Locate every blood parasite and identify its species.
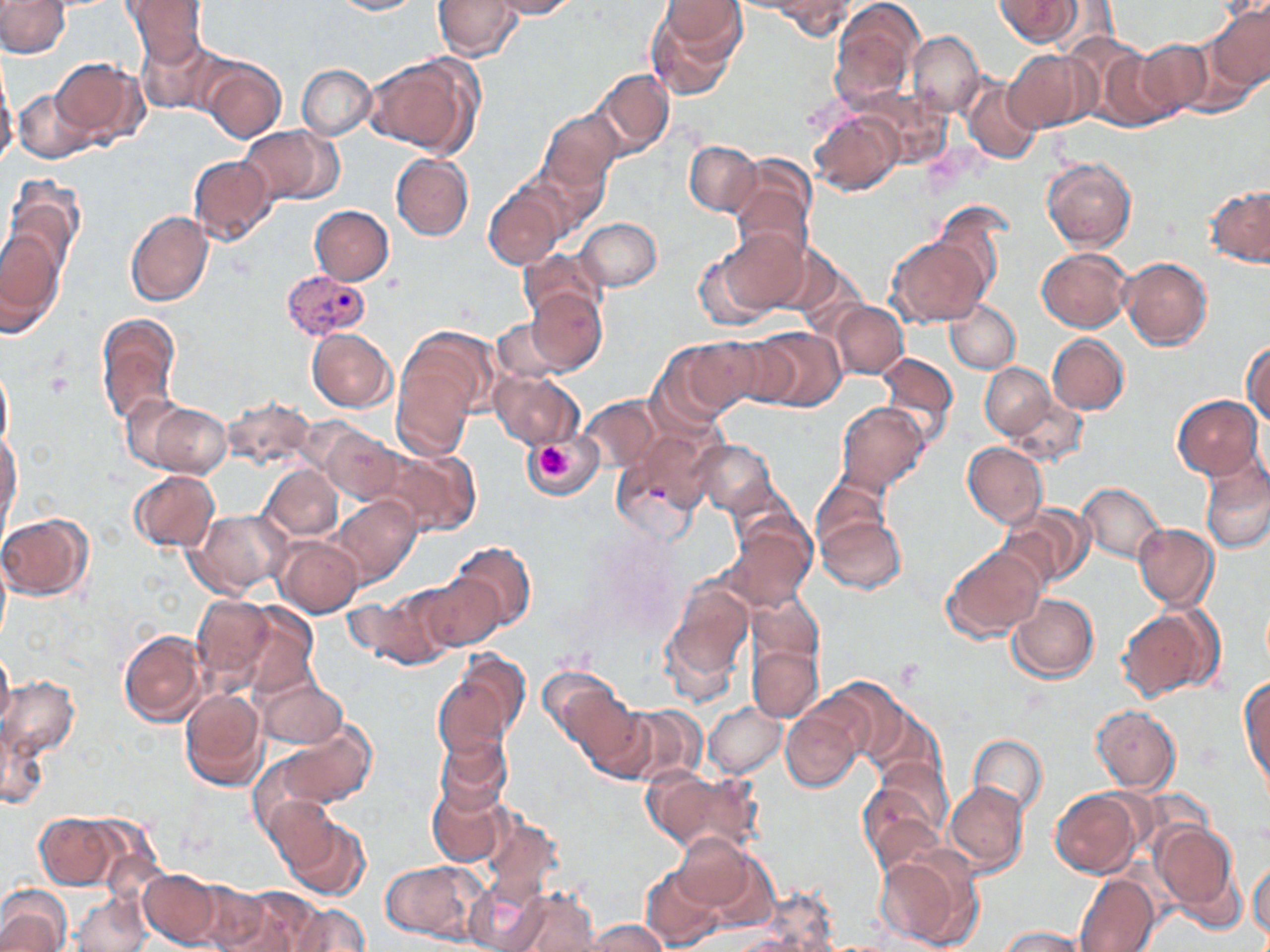
Approximate bounding boxes as named x1/y1/x2/y2 corners in pixels.
Plasmodium vivax-infected red blood cells: (x1=282, y1=269, x2=372, y2=343).
No Plasmodium falciparum, Plasmodium ovale, Plasmodium malariae, Babesia divergens, or Trypanosoma brucei observed.

Summary:
  - Uninfected red blood cell locations: (x1=0, y1=0, x2=70, y2=57), (x1=121, y1=0, x2=211, y2=64), (x1=434, y1=0, x2=523, y2=61), (x1=486, y1=0, x2=579, y2=18), (x1=829, y1=0, x2=923, y2=107), (x1=994, y1=0, x2=1083, y2=46), (x1=330, y1=1, x2=422, y2=15), (x1=645, y1=1, x2=747, y2=99), (x1=772, y1=1, x2=855, y2=38), (x1=1207, y1=2, x2=1270, y2=94), (x1=1183, y1=24, x2=1263, y2=117), (x1=907, y1=30, x2=985, y2=117), (x1=135, y1=35, x2=230, y2=117), (x1=1131, y1=40, x2=1211, y2=121), (x1=1087, y1=44, x2=1175, y2=130), (x1=1004, y1=49, x2=1094, y2=133), (x1=364, y1=53, x2=482, y2=160), (x1=51, y1=56, x2=147, y2=146), (x1=201, y1=56, x2=286, y2=141), (x1=296, y1=63, x2=376, y2=140), (x1=0, y1=65, x2=17, y2=169), (x1=593, y1=68, x2=674, y2=158), (x1=963, y1=79, x2=1042, y2=163), (x1=13, y1=88, x2=93, y2=164), (x1=807, y1=104, x2=906, y2=197), (x1=538, y1=107, x2=625, y2=196), (x1=238, y1=125, x2=342, y2=207), (x1=685, y1=139, x2=763, y2=216), (x1=524, y1=146, x2=614, y2=234), (x1=391, y1=153, x2=473, y2=240), (x1=187, y1=154, x2=276, y2=245), (x1=730, y1=156, x2=816, y2=249), (x1=1042, y1=157, x2=1138, y2=252), (x1=3, y1=178, x2=84, y2=286), (x1=484, y1=181, x2=568, y2=269), (x1=1205, y1=185, x2=1270, y2=266), (x1=310, y1=205, x2=394, y2=284), (x1=125, y1=210, x2=213, y2=306), (x1=576, y1=217, x2=661, y2=292), (x1=701, y1=224, x2=812, y2=324), (x1=0, y1=225, x2=65, y2=327), (x1=888, y1=235, x2=990, y2=325), (x1=518, y1=246, x2=606, y2=331), (x1=1037, y1=247, x2=1134, y2=331), (x1=1119, y1=257, x2=1213, y2=349), (x1=523, y1=285, x2=606, y2=375), (x1=831, y1=300, x2=907, y2=379), (x1=944, y1=301, x2=1021, y2=374), (x1=95, y1=312, x2=182, y2=427), (x1=490, y1=319, x2=571, y2=388), (x1=392, y1=326, x2=501, y2=449), (x1=754, y1=326, x2=844, y2=412), (x1=307, y1=328, x2=397, y2=412), (x1=1048, y1=333, x2=1130, y2=414), (x1=667, y1=336, x2=769, y2=419), (x1=1242, y1=340, x2=1270, y2=427), (x1=875, y1=351, x2=959, y2=448), (x1=0, y1=362, x2=13, y2=453), (x1=980, y1=362, x2=1060, y2=442), (x1=490, y1=370, x2=584, y2=449), (x1=128, y1=394, x2=233, y2=476), (x1=578, y1=395, x2=663, y2=475), (x1=1173, y1=396, x2=1261, y2=478), (x1=835, y1=402, x2=929, y2=493), (x1=315, y1=421, x2=406, y2=504), (x1=612, y1=430, x2=713, y2=542), (x1=0, y1=431, x2=21, y2=531), (x1=523, y1=433, x2=603, y2=498), (x1=684, y1=437, x2=782, y2=517), (x1=373, y1=440, x2=481, y2=536), (x1=963, y1=441, x2=1047, y2=526), (x1=1200, y1=458, x2=1269, y2=553), (x1=262, y1=465, x2=343, y2=543), (x1=129, y1=469, x2=220, y2=551), (x1=1077, y1=481, x2=1165, y2=563), (x1=811, y1=495, x2=909, y2=597), (x1=329, y1=496, x2=419, y2=587), (x1=1001, y1=504, x2=1093, y2=590), (x1=184, y1=507, x2=296, y2=599), (x1=0, y1=512, x2=93, y2=600), (x1=724, y1=514, x2=815, y2=612), (x1=1134, y1=522, x2=1218, y2=609), (x1=275, y1=536, x2=363, y2=616), (x1=445, y1=538, x2=537, y2=637), (x1=943, y1=543, x2=1047, y2=641), (x1=0, y1=557, x2=10, y2=639), (x1=412, y1=571, x2=505, y2=653), (x1=349, y1=578, x2=458, y2=666), (x1=661, y1=578, x2=755, y2=698), (x1=191, y1=591, x2=297, y2=697), (x1=1007, y1=592, x2=1099, y2=682), (x1=1116, y1=604, x2=1223, y2=702), (x1=110, y1=615, x2=292, y2=715), (x1=118, y1=628, x2=209, y2=725), (x1=747, y1=640, x2=822, y2=722), (x1=0, y1=646, x2=14, y2=730), (x1=432, y1=655, x2=527, y2=761), (x1=540, y1=666, x2=634, y2=760), (x1=253, y1=669, x2=350, y2=752), (x1=1, y1=673, x2=79, y2=765), (x1=1239, y1=673, x2=1269, y2=791), (x1=180, y1=684, x2=269, y2=791), (x1=781, y1=698, x2=869, y2=793), (x1=601, y1=699, x2=707, y2=785), (x1=703, y1=702, x2=787, y2=776), (x1=1091, y1=704, x2=1180, y2=793), (x1=2, y1=713, x2=50, y2=814), (x1=262, y1=719, x2=376, y2=813), (x1=431, y1=732, x2=514, y2=821), (x1=968, y1=734, x2=1048, y2=817), (x1=859, y1=760, x2=952, y2=868), (x1=643, y1=765, x2=760, y2=857), (x1=427, y1=776, x2=510, y2=869), (x1=945, y1=782, x2=1027, y2=876), (x1=1049, y1=787, x2=1147, y2=877), (x1=274, y1=807, x2=369, y2=900), (x1=32, y1=811, x2=140, y2=890), (x1=1151, y1=819, x2=1243, y2=924), (x1=672, y1=832, x2=770, y2=922), (x1=874, y1=848, x2=978, y2=949), (x1=380, y1=858, x2=488, y2=941), (x1=1248, y1=860, x2=1269, y2=941), (x1=641, y1=865, x2=727, y2=949), (x1=139, y1=868, x2=229, y2=949), (x1=459, y1=873, x2=556, y2=952), (x1=1073, y1=873, x2=1160, y2=952), (x1=0, y1=885, x2=73, y2=952), (x1=505, y1=886, x2=603, y2=952), (x1=212, y1=887, x2=329, y2=952), (x1=71, y1=890, x2=151, y2=952), (x1=284, y1=902, x2=370, y2=951), (x1=581, y1=919, x2=671, y2=952), (x1=995, y1=926, x2=1091, y2=951)
  - Platelet locations: (x1=46, y1=372, x2=74, y2=398), (x1=537, y1=445, x2=569, y2=479), (x1=896, y1=659, x2=921, y2=689)
  - Slide-level diagnosis: Plasmodium vivax
  - Modality: optical microscopy
  - Magnification: 1000x
  - Image size: 1270×952 pixels
  - Field of view: single
  - Stain: May-Grünwald-Giemsa
  - Preparation: thin blood film